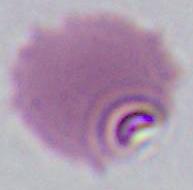

Captured at either 400x or 1000x magnification. Photomicrograph. A Plasmodium parasite is seen.